Report the malaria status of this cell.
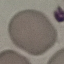

Uninfected.

Summary:
  - Capture: smartphone camera at the microscope eyepiece
  - Stain: Giemsa
  - Preparation: thin blood film
  - Image type: cell patch, automatically extracted from a larger field of view and resized to 64 × 64 pixels